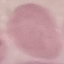

{
  "malaria_status": "uninfected",
  "capture": "smartphone through the microscope eyepiece",
  "preparation": "thin blood smear",
  "stain": "Giemsa",
  "image_type": "automatically extracted cell patch, resized to 64 × 64 pixels"
}